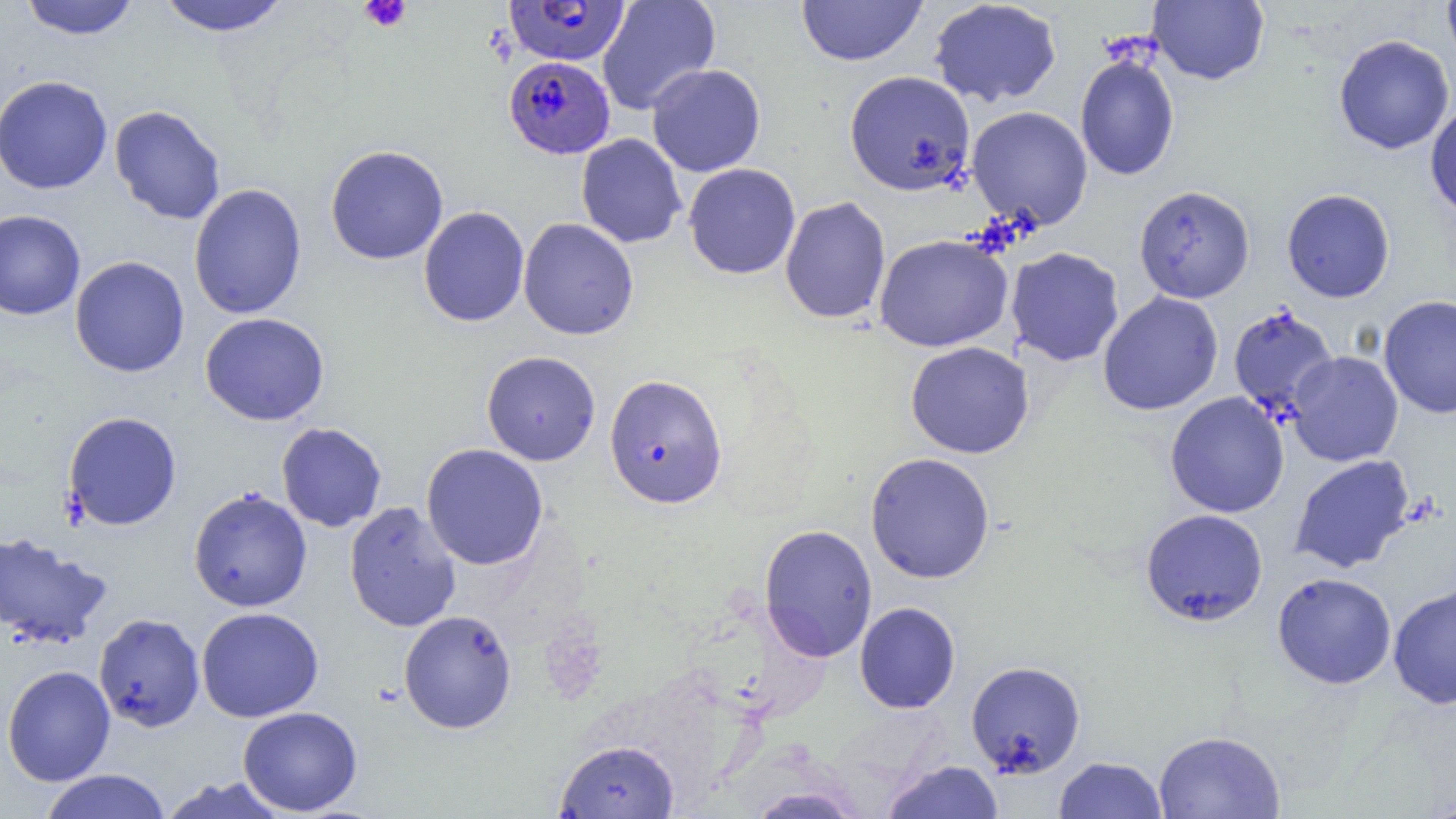
Approximate bounding boxes as (x1, y1, x2, y2) in pixels. Uninfected red blood cell locations: (18, 0, 140, 40), (156, 0, 291, 37), (597, 0, 721, 115), (796, 0, 927, 66), (928, 0, 1062, 108), (1442, 0, 1456, 72), (1148, 1, 1269, 85), (1333, 34, 1455, 155), (1075, 52, 1180, 181), (646, 63, 766, 177), (846, 70, 977, 196), (0, 75, 113, 195), (1425, 102, 1456, 220), (109, 105, 226, 224), (967, 106, 1093, 230), (576, 133, 687, 248), (324, 145, 449, 265), (683, 163, 801, 279), (189, 183, 307, 320), (1134, 185, 1255, 303), (1281, 189, 1395, 303), (780, 196, 891, 324), (418, 206, 530, 327), (0, 210, 86, 320), (518, 218, 639, 340), (873, 234, 1013, 352), (1006, 247, 1124, 366), (70, 256, 190, 378), (1097, 291, 1223, 416), (1378, 295, 1456, 418), (1227, 306, 1339, 420), (200, 312, 330, 426), (905, 341, 1034, 459), (481, 350, 601, 466), (1287, 351, 1403, 466), (1165, 392, 1290, 518), (63, 411, 182, 531), (276, 422, 387, 531), (421, 443, 549, 570), (865, 452, 995, 583), (1290, 455, 1416, 574), (188, 487, 313, 612), (344, 501, 462, 632), (1140, 508, 1269, 626), (759, 524, 878, 661), (0, 530, 112, 649), (1272, 572, 1397, 689), (1388, 583, 1456, 709), (854, 601, 961, 714), (196, 606, 324, 722), (398, 610, 517, 734), (93, 612, 205, 731), (965, 660, 1086, 777), (2, 664, 115, 786), (238, 706, 362, 816), (1154, 730, 1285, 818), (555, 739, 680, 818), (1054, 756, 1167, 818), (881, 760, 1004, 819), (38, 769, 172, 819), (157, 776, 292, 819), (746, 786, 866, 818). Plasmodium falciparum-infected red blood cell locations: (504, 0, 630, 66), (504, 55, 615, 159), (604, 374, 727, 509). Platelet locations: (358, 0, 411, 32). Slide-level diagnosis: Plasmodium falciparum. Captured at 1000x magnification. Image is 1456×819 pixels. Single field of view. Light microscopy. Thin blood smear.